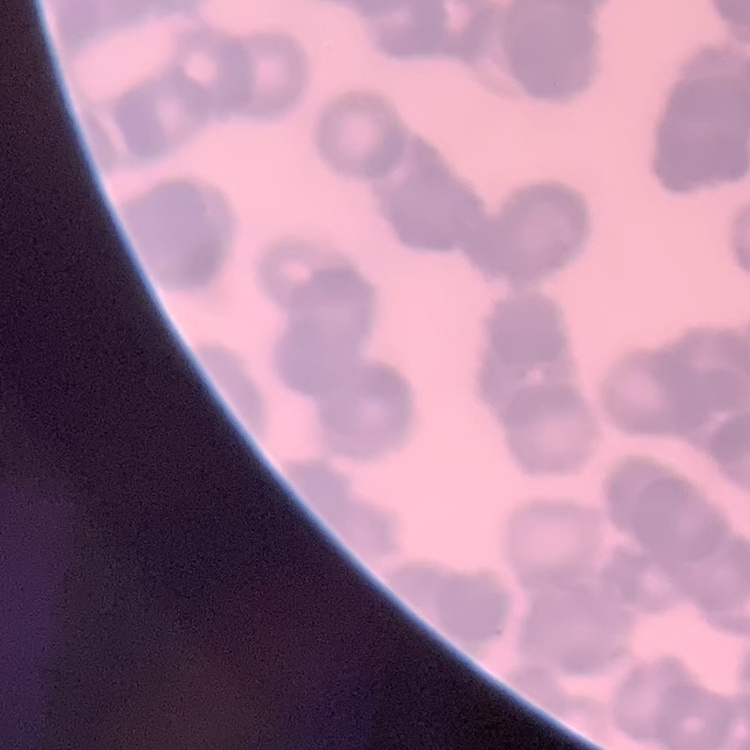
Summary:
  - Red blood cell morphology: rouleaux formation
  - Image type: one tile cut from a larger photomicrograph
  - Stain: Field's or Giemsa
  - Preparation: thin blood film